Report the malaria status of this cell.
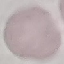

It is uninfected.

Summary:
  - Stain: Giemsa
  - Preparation: thin smear
  - Capture: smartphone camera at the microscope eyepiece
  - Image type: automatically extracted cell patch, resized to 64 × 64 pixels